Find each white blood cell.
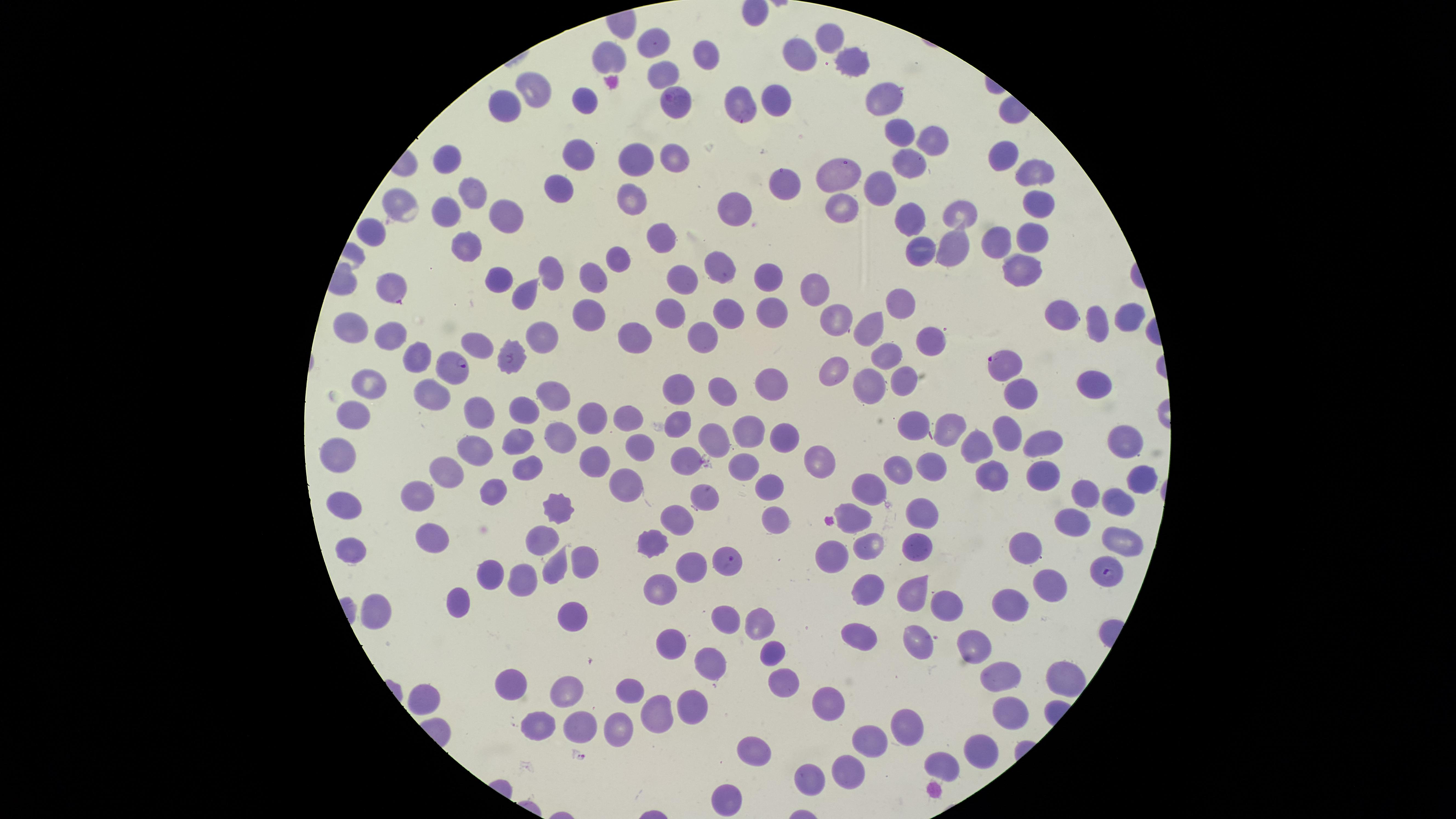
No white blood cells identified.

Approximate marker points as {x, y} in pixels. Parasitized red blood cells: {673, 99}, {391, 287}, {1000, 362}, {452, 367}, {725, 558}, {1108, 575}. Uninfected red blood cells: {827, 37}, {653, 45}, {604, 58}, {707, 58}, {849, 58}, {798, 62}, {657, 76}, {531, 91}, {584, 96}, {772, 97}, {882, 101}, {503, 104}, {738, 105}, {895, 132}, {925, 140}, {570, 151}, {673, 153}, {631, 156}, {1005, 156}, {442, 162}, {905, 165}, {1035, 171}, {837, 177}, {783, 186}, {555, 187}, {880, 192}, {469, 195}, {630, 196}, {1034, 199}, {402, 206}, {732, 206}, {842, 209}, {449, 210}, {507, 213}, {961, 213}, {908, 216}, {370, 228}, {661, 236}, {1023, 237}, {467, 247}, {922, 247}, {1001, 248}, {952, 250}, {618, 255}, {724, 269}, {1023, 270}, {492, 272}, {545, 274}, {764, 276}, {596, 280}, {690, 281}, {810, 284}, {524, 296}, {894, 301}, {732, 307}, {673, 311}, {1125, 314}, {770, 315}, {594, 316}, {1057, 316}, {834, 321}, {1096, 323}, {874, 331}, {351, 334}, {380, 335}, {637, 336}, {922, 338}, {702, 340}, {544, 341}, {472, 345}, {886, 353}, {416, 355}, {509, 356}, {833, 373}, {902, 376}, {775, 382}, {1096, 384}, {369, 387}, {871, 387}, {679, 388}, {722, 389}, {431, 394}, {556, 396}, {1016, 399}, {524, 401}, {479, 411}, {353, 414}, {592, 421}, {627, 421}, {951, 421}, {676, 423}, {909, 425}, {1003, 432}, {744, 433}, {711, 435}, {1121, 436}, {562, 439}, {774, 439}, {1043, 442}, {516, 444}, {971, 446}, {636, 447}, {473, 451}, {342, 454}, {821, 455}, {685, 458}, {524, 465}, {592, 465}, {744, 467}, {897, 471}, {929, 471}, {446, 472}, {1046, 475}, {1132, 478}, {989, 480}, {623, 485}, {766, 485}, {863, 485}, {491, 492}, {704, 492}, {1088, 493}, {414, 496}, {1115, 498}, {343, 502}, {553, 508}, {855, 516}, {919, 519}, {1070, 519}, {677, 520}, {776, 524}, {429, 535}, {1117, 537}, {536, 539}, {871, 541}, {914, 546}, {654, 547}, {1027, 548}, {348, 553}, {830, 554}, {577, 562}, {550, 566}, {690, 566}, {489, 570}, {1054, 580}, {516, 582}, {867, 585}, {658, 587}, {907, 589}, {456, 594}, {1006, 600}, {948, 606}, {377, 609}, {725, 620}, {757, 622}, {570, 628}, {855, 635}, {672, 640}, {919, 643}, {979, 643}, {772, 652}, {702, 662}, {998, 672}, {1061, 672}, {778, 682}, {512, 684}, {567, 691}, {422, 694}, {632, 694}, {688, 704}, {827, 704}, {1002, 705}, {652, 719}, {583, 721}, {912, 723}, {537, 725}, {621, 726}, {870, 737}, {759, 751}, {979, 751}, {943, 764}, {849, 766}, {810, 778}, {724, 797}. The visible region is circular. Image is 1456×819 pixels. Giemsa-stained preparation. Smartphone photograph through the microscope eyepiece. Thin blood smear. Single field of view. Species: Plasmodium falciparum. Presence: malaria parasites identified.